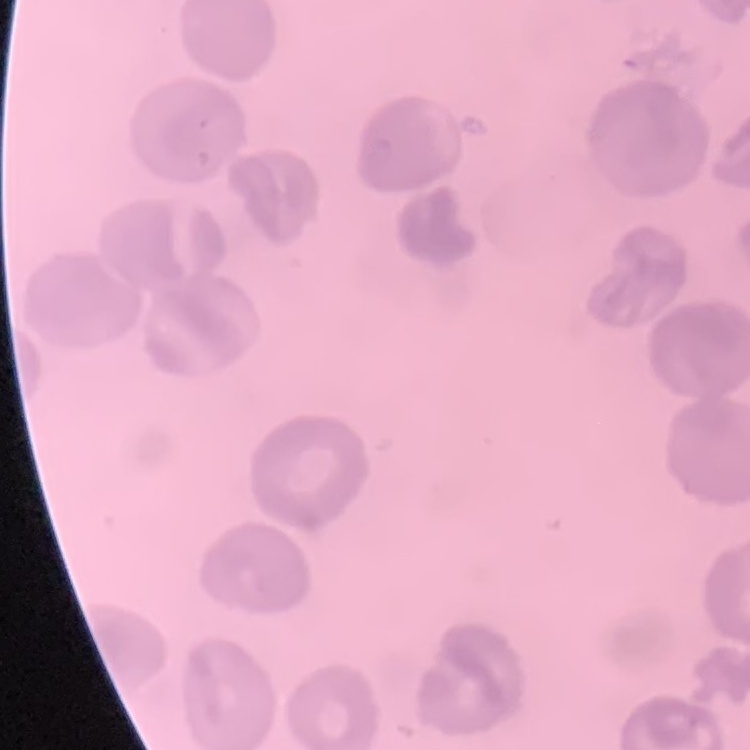

{
  "red_blood_cell_morphology": "no rouleaux formation",
  "stain": "Field's or Giemsa",
  "preparation": "thin blood smear",
  "image_type": "square crop of a larger photomicrograph"
}